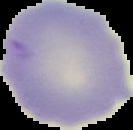
The area outside the segmented cell region is set to black. Image is 133×130 pixels. From a thin blood film. Malaria status: uninfected.